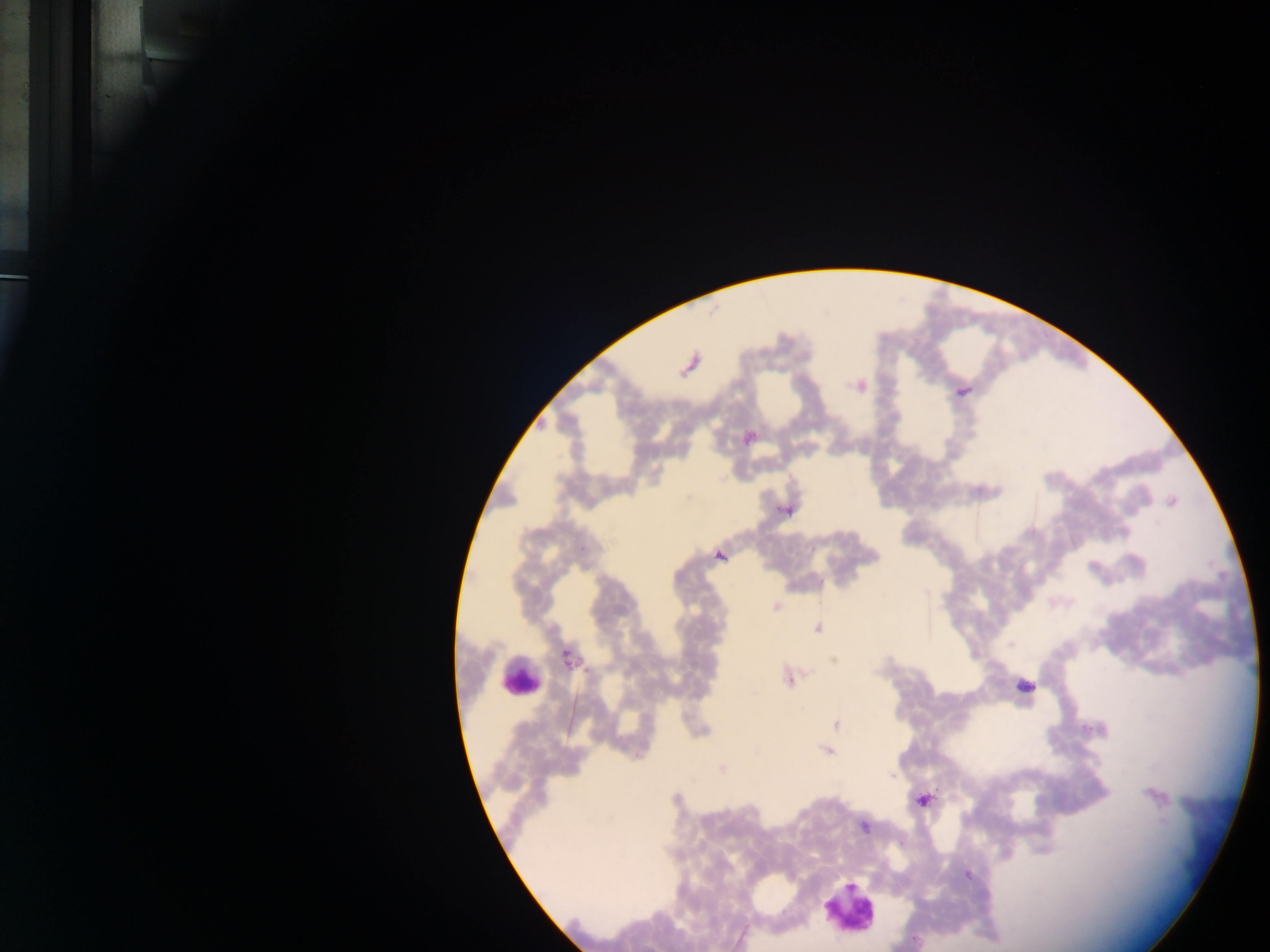
Approximate centers as x y in pixels.
Summary:
  - Malaria parasite locations: 690 364; 858 385; 962 391; 749 436; 1171 501; 787 510; 719 555; 776 606; 818 628; 567 657; 834 660; 788 677; 1024 686; 836 724; 827 751; 722 769; 1154 795; 922 800; 865 826; 967 874; 916 941
  - Leukocyte locations: 520 678; 849 911
  - Image size: 1270×952 pixels
  - Field of view: single
  - Country: Ghana
  - Preparation: thick blood smear
  - Capture: mobile-phone photograph through a microscope